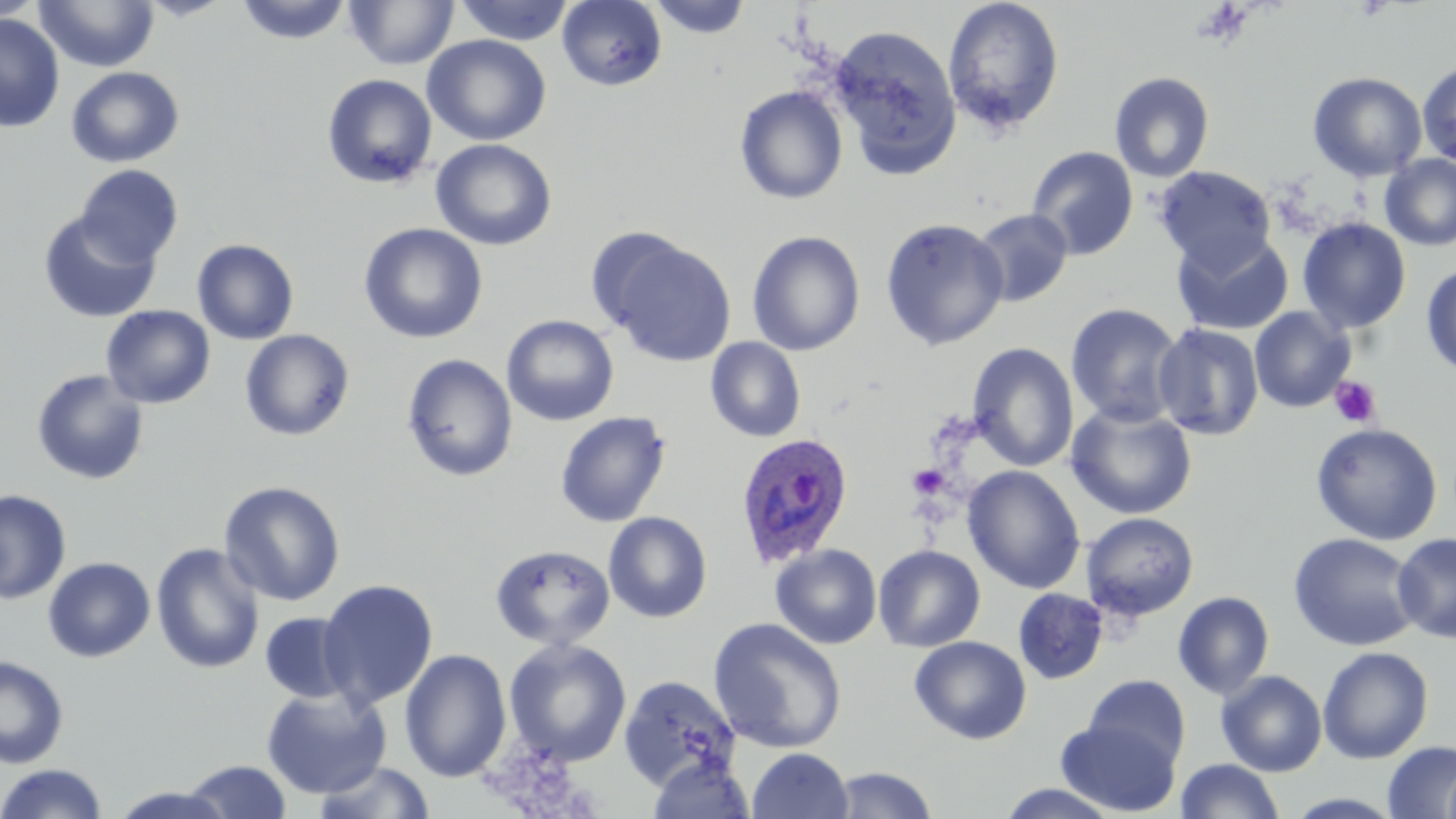
Approximate bounding boxes as [x1, y1, x2, y2] in pixels. Platelet locations: [1330, 376, 1382, 427], [907, 464, 948, 498]. Uninfected red blood cell locations: [0, 0, 45, 21], [34, 0, 160, 72], [138, 0, 233, 21], [236, 0, 352, 45], [454, 0, 575, 46], [557, 0, 668, 91], [648, 0, 752, 39], [942, 0, 1065, 136], [344, 1, 460, 70], [0, 13, 65, 133], [828, 23, 963, 177], [422, 35, 552, 146], [1417, 60, 1456, 167], [66, 66, 184, 168], [1109, 71, 1215, 182], [1307, 71, 1428, 182], [321, 74, 437, 189], [734, 85, 848, 205], [430, 138, 556, 251], [1026, 146, 1139, 260], [1380, 154, 1456, 251], [76, 164, 183, 267], [1154, 165, 1276, 272], [970, 209, 1074, 308], [38, 210, 161, 323], [879, 217, 1009, 351], [1297, 217, 1411, 334], [358, 223, 488, 344], [746, 230, 866, 356], [1171, 231, 1294, 335], [600, 235, 736, 366], [192, 239, 299, 345], [1421, 264, 1456, 379], [1065, 303, 1185, 427], [100, 305, 215, 409], [1249, 307, 1356, 413], [501, 314, 619, 426], [1152, 322, 1265, 441], [239, 329, 355, 441], [705, 337, 806, 443], [967, 342, 1079, 472], [401, 353, 518, 482], [30, 368, 150, 486], [1065, 403, 1198, 520], [555, 411, 672, 527], [1310, 422, 1444, 546], [963, 465, 1086, 594], [219, 480, 346, 607], [0, 489, 71, 604], [603, 512, 712, 623], [1081, 512, 1199, 621], [1392, 531, 1456, 643], [1288, 532, 1422, 651], [150, 542, 265, 675], [490, 543, 616, 651], [770, 543, 882, 649], [873, 544, 986, 652], [42, 557, 155, 662], [317, 578, 438, 709], [1014, 588, 1108, 685], [1172, 591, 1275, 699], [259, 612, 358, 704], [708, 617, 848, 755], [909, 636, 1032, 745], [504, 639, 632, 766], [1317, 646, 1434, 763], [399, 649, 512, 782], [0, 655, 69, 769], [1216, 670, 1327, 777], [618, 674, 742, 791], [1083, 675, 1191, 773], [261, 687, 391, 799], [1055, 718, 1180, 816], [1382, 740, 1456, 819], [747, 748, 854, 819], [646, 755, 756, 818], [1176, 758, 1285, 818], [182, 759, 292, 818], [312, 759, 437, 818], [1443, 759, 1456, 819], [0, 763, 109, 819], [829, 766, 939, 818], [995, 783, 1123, 818], [108, 786, 237, 819], [1281, 792, 1406, 818]. Plasmodium ovale-infected red blood cell locations: [735, 431, 855, 568]. Slide-level diagnosis: Plasmodium ovale. Thin blood film. May-Grünwald-Giemsa stain. Light microscopy. Single field of view. Captured at 1000x magnification. Image is 1456×819 pixels.